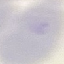 Result: no malaria parasites detected. Acquired by smartphone through the microscope eyepiece. Thin smear of blood. Automatically extracted cell patch, resized to 64 × 64 pixels. Giemsa stain.